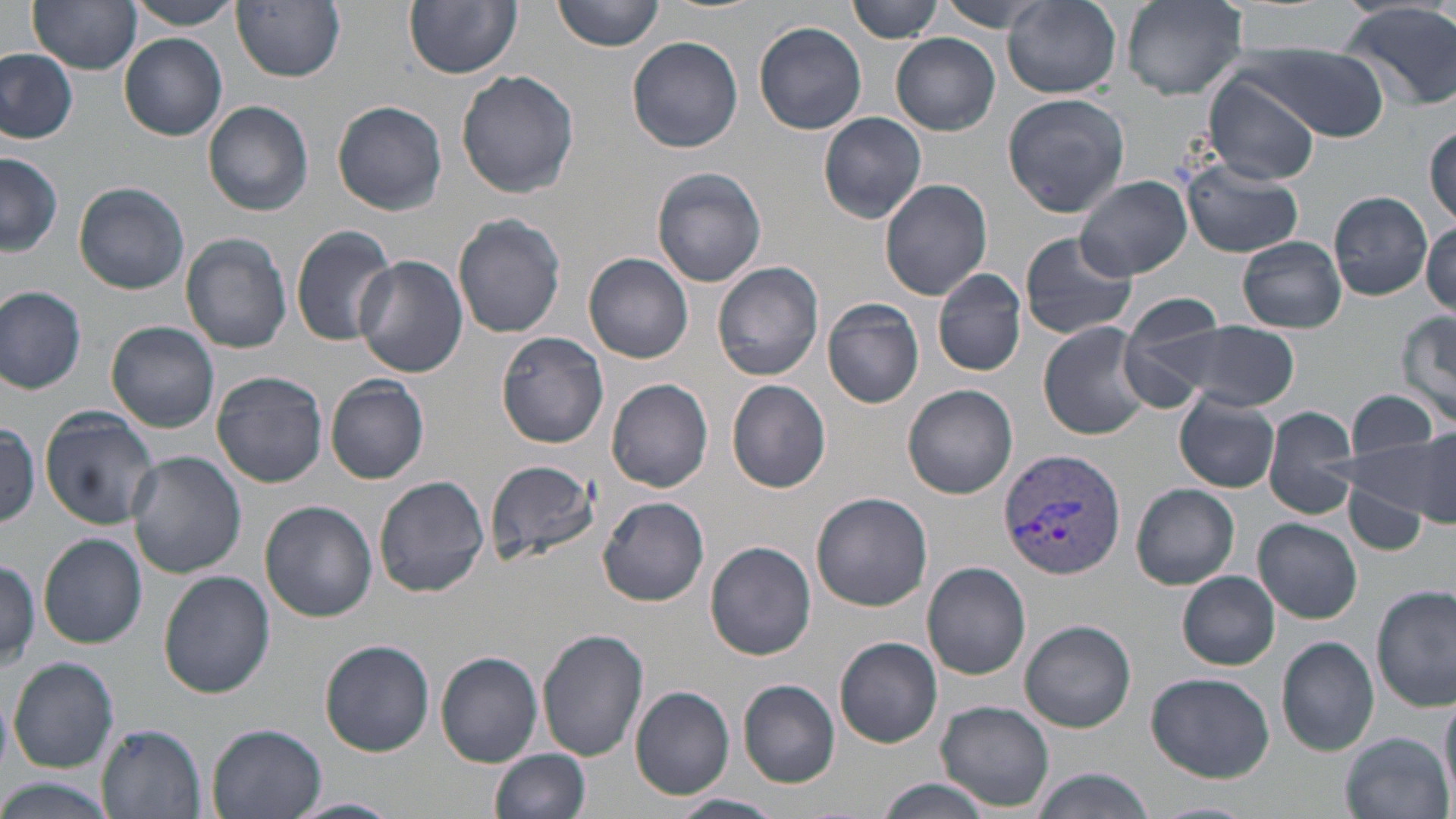

Summary:
  - Coordinate format: approximate bounding boxes as named x1/y1/x2/y2 corners in pixels
  - Uninfected red blood cell locations: (x1=29, y1=0, x2=143, y2=73), (x1=125, y1=0, x2=243, y2=30), (x1=405, y1=0, x2=522, y2=78), (x1=554, y1=0, x2=665, y2=52), (x1=849, y1=0, x2=943, y2=44), (x1=936, y1=0, x2=1061, y2=33), (x1=1005, y1=0, x2=1121, y2=99), (x1=1121, y1=0, x2=1247, y2=99), (x1=233, y1=1, x2=347, y2=81), (x1=1337, y1=1, x2=1456, y2=109), (x1=755, y1=20, x2=869, y2=133), (x1=120, y1=33, x2=227, y2=140), (x1=891, y1=35, x2=1000, y2=135), (x1=628, y1=36, x2=744, y2=152), (x1=1233, y1=41, x2=1392, y2=141), (x1=0, y1=48, x2=79, y2=144), (x1=456, y1=68, x2=582, y2=199), (x1=1207, y1=75, x2=1321, y2=186), (x1=1002, y1=93, x2=1130, y2=216), (x1=333, y1=99, x2=448, y2=215), (x1=202, y1=100, x2=315, y2=216), (x1=819, y1=112, x2=928, y2=223), (x1=1427, y1=123, x2=1456, y2=224), (x1=0, y1=152, x2=62, y2=257), (x1=1180, y1=157, x2=1303, y2=259), (x1=652, y1=168, x2=767, y2=286), (x1=1075, y1=175, x2=1193, y2=280), (x1=880, y1=179, x2=993, y2=300), (x1=75, y1=181, x2=190, y2=294), (x1=1329, y1=191, x2=1433, y2=300), (x1=454, y1=212, x2=567, y2=339), (x1=1421, y1=220, x2=1456, y2=316), (x1=290, y1=225, x2=397, y2=345), (x1=1019, y1=230, x2=1139, y2=341), (x1=181, y1=232, x2=294, y2=354), (x1=1237, y1=237, x2=1346, y2=333), (x1=584, y1=252, x2=695, y2=363), (x1=355, y1=255, x2=470, y2=380), (x1=713, y1=262, x2=825, y2=381), (x1=933, y1=269, x2=1026, y2=377), (x1=0, y1=287, x2=87, y2=395), (x1=822, y1=298, x2=925, y2=408), (x1=1116, y1=299, x2=1250, y2=406), (x1=1394, y1=309, x2=1456, y2=427), (x1=1157, y1=319, x2=1298, y2=414), (x1=107, y1=321, x2=220, y2=432), (x1=1037, y1=321, x2=1157, y2=441), (x1=495, y1=331, x2=609, y2=448), (x1=211, y1=370, x2=328, y2=487), (x1=325, y1=376, x2=430, y2=484), (x1=606, y1=377, x2=715, y2=492), (x1=726, y1=379, x2=833, y2=494), (x1=902, y1=384, x2=1018, y2=499), (x1=1345, y1=389, x2=1439, y2=462), (x1=1174, y1=393, x2=1282, y2=494), (x1=1262, y1=403, x2=1360, y2=519), (x1=40, y1=408, x2=158, y2=529), (x1=0, y1=422, x2=44, y2=526), (x1=1408, y1=424, x2=1456, y2=525), (x1=1348, y1=432, x2=1452, y2=519), (x1=127, y1=452, x2=247, y2=577), (x1=483, y1=457, x2=601, y2=566), (x1=373, y1=475, x2=490, y2=597), (x1=1343, y1=482, x2=1429, y2=554), (x1=1132, y1=484, x2=1240, y2=589), (x1=811, y1=491, x2=933, y2=612), (x1=597, y1=497, x2=710, y2=606), (x1=260, y1=500, x2=378, y2=622), (x1=1255, y1=518, x2=1362, y2=622), (x1=40, y1=534, x2=147, y2=650), (x1=705, y1=540, x2=818, y2=661), (x1=0, y1=558, x2=40, y2=668), (x1=921, y1=561, x2=1031, y2=680), (x1=159, y1=570, x2=274, y2=697), (x1=1178, y1=572, x2=1279, y2=669), (x1=1373, y1=586, x2=1453, y2=714), (x1=1021, y1=621, x2=1136, y2=732), (x1=537, y1=628, x2=650, y2=760), (x1=1276, y1=635, x2=1379, y2=756), (x1=833, y1=636, x2=943, y2=748), (x1=319, y1=640, x2=435, y2=756), (x1=434, y1=650, x2=543, y2=768), (x1=8, y1=657, x2=118, y2=772), (x1=1147, y1=671, x2=1274, y2=782), (x1=738, y1=679, x2=841, y2=787), (x1=630, y1=686, x2=736, y2=800), (x1=1, y1=689, x2=13, y2=775), (x1=1440, y1=690, x2=1456, y2=801), (x1=936, y1=701, x2=1055, y2=811), (x1=96, y1=721, x2=208, y2=818), (x1=205, y1=722, x2=328, y2=819), (x1=1341, y1=732, x2=1452, y2=817), (x1=490, y1=749, x2=591, y2=819), (x1=1029, y1=768, x2=1154, y2=819), (x1=875, y1=777, x2=993, y2=819), (x1=0, y1=779, x2=118, y2=819), (x1=672, y1=793, x2=783, y2=819), (x1=287, y1=795, x2=400, y2=819), (x1=1150, y1=800, x2=1261, y2=818)
  - Plasmodium vivax-infected red blood cell locations: (x1=996, y1=446, x2=1130, y2=579)
  - Slide-level diagnosis: Plasmodium vivax
  - Magnification: 1000x
  - Image size: 1456×819 pixels
  - Stain: May-Grünwald-Giemsa
  - Modality: optical microscopy
  - Field of view: single
  - Preparation: thin blood film